Outline each blood parasite and name the species.
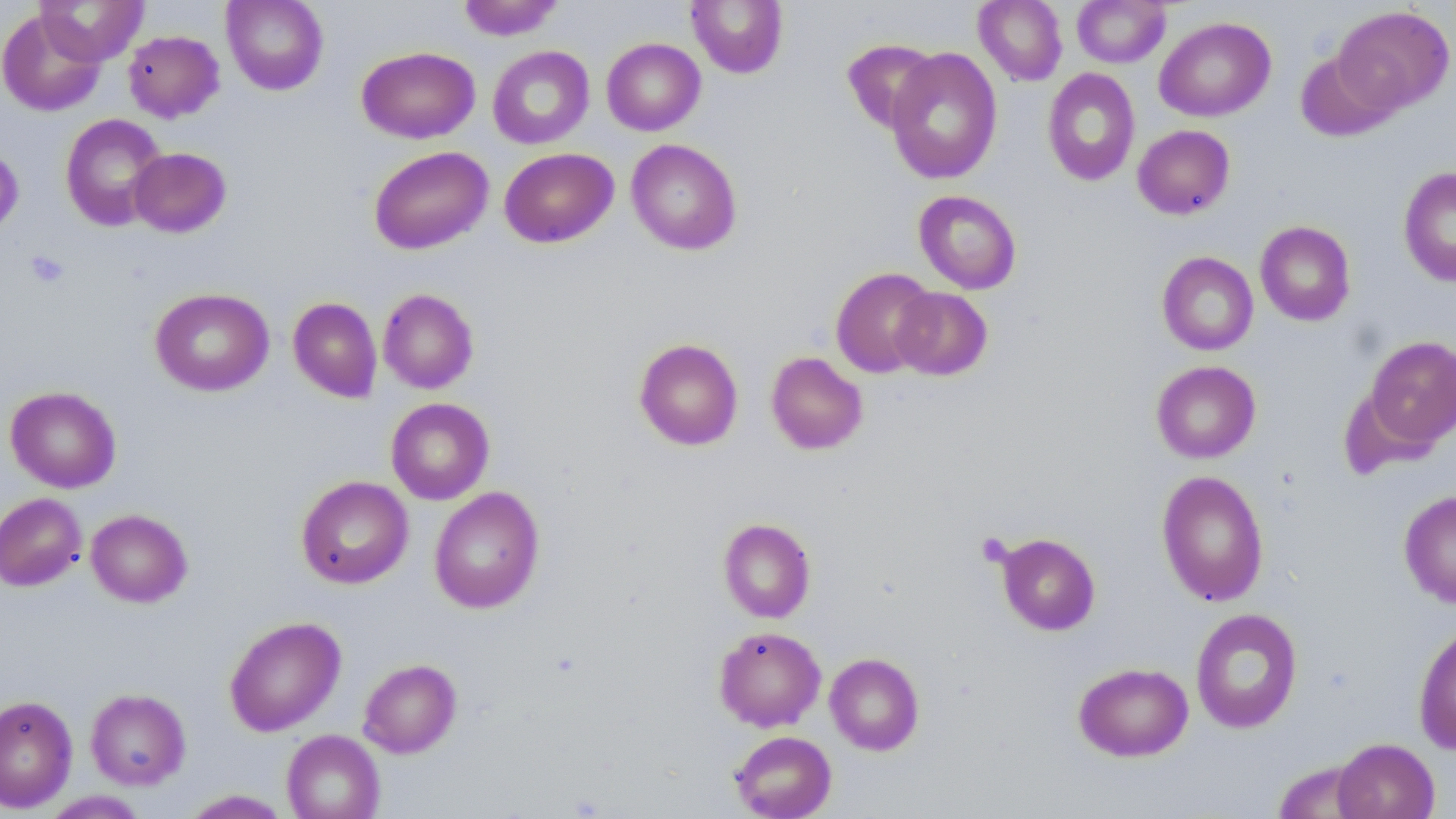
No blood parasites observed.

Summary:
  - Coordinate format: approximate bounding boxes as [x1, y1, x2, y2] in pixels
  - Platelet locations: [26, 250, 69, 288], [976, 533, 1013, 568]
  - Uninfected red blood cell locations: [35, 0, 148, 65], [222, 0, 329, 95], [456, 0, 565, 40], [686, 0, 789, 79], [974, 0, 1068, 86], [1072, 0, 1171, 68], [1332, 5, 1455, 114], [0, 9, 105, 116], [1154, 16, 1276, 122], [123, 30, 224, 122], [602, 37, 705, 136], [842, 38, 940, 134], [487, 45, 595, 149], [357, 46, 480, 143], [885, 48, 1003, 184], [1294, 51, 1400, 143], [1043, 68, 1140, 186], [59, 113, 168, 231], [1132, 124, 1235, 219], [626, 139, 742, 255], [0, 144, 24, 239], [368, 146, 493, 254], [129, 147, 231, 237], [499, 147, 619, 248], [1398, 165, 1456, 288], [913, 190, 1022, 294], [1255, 221, 1356, 326], [1157, 251, 1258, 355], [830, 267, 938, 378], [150, 287, 274, 396], [891, 287, 993, 380], [378, 288, 479, 394], [288, 297, 382, 403], [1363, 335, 1456, 450], [634, 338, 744, 451], [766, 351, 868, 455], [1151, 360, 1261, 463], [5, 386, 121, 493], [385, 397, 495, 505], [1156, 470, 1269, 607], [296, 475, 413, 589], [429, 486, 545, 613], [1399, 489, 1456, 608], [0, 493, 87, 591], [85, 508, 193, 607], [718, 518, 816, 623], [996, 533, 1101, 635], [1190, 607, 1303, 733], [224, 615, 346, 736], [1413, 624, 1456, 754], [714, 626, 826, 732], [825, 652, 924, 755], [358, 658, 462, 758], [1073, 662, 1194, 761], [85, 688, 191, 790], [0, 695, 77, 813], [281, 729, 385, 819], [729, 731, 837, 819], [1332, 738, 1440, 819], [1272, 760, 1373, 818], [180, 789, 292, 818], [39, 791, 149, 818]
  - Slide-level diagnosis: negative for blood parasites
  - Image size: 1456×819 pixels
  - Field of view: single
  - Modality: optical microscopy
  - Stain: May-Grünwald-Giemsa
  - Magnification: 1000x
  - Preparation: thin blood film